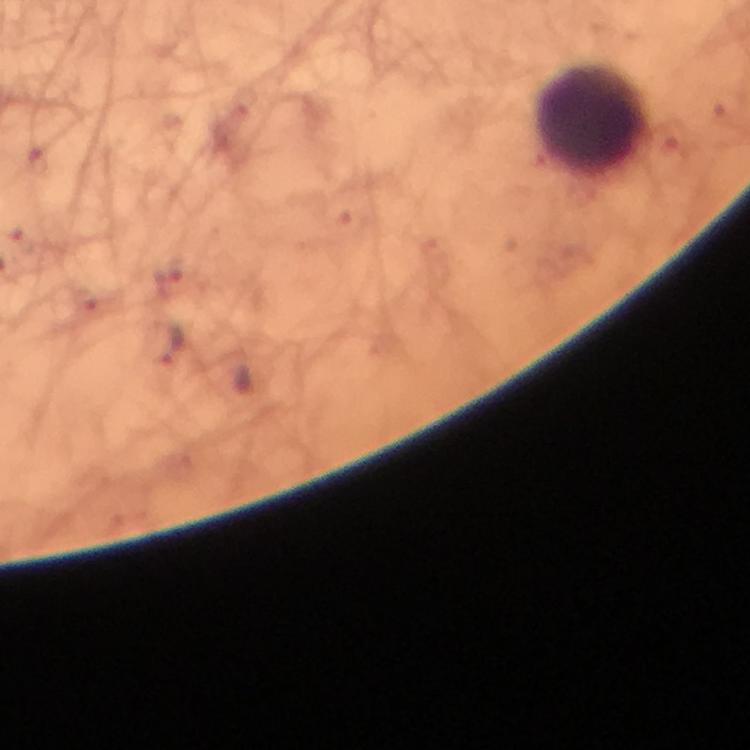

Approximate centers as (x, y) in pixels.
Summary:
  - Malaria parasite locations: (168, 344)
  - Leukocyte locations: (594, 121)
  - Capture: smartphone mounted on the microscope
  - Magnification: 100x
  - Context: from a diagnostic examination for malaria
  - Cropped from: a single field of view
  - Stain: Giemsa
  - Image size: 750×750 pixels
  - Immersion oil: applied
  - Preparation: thick blood smear